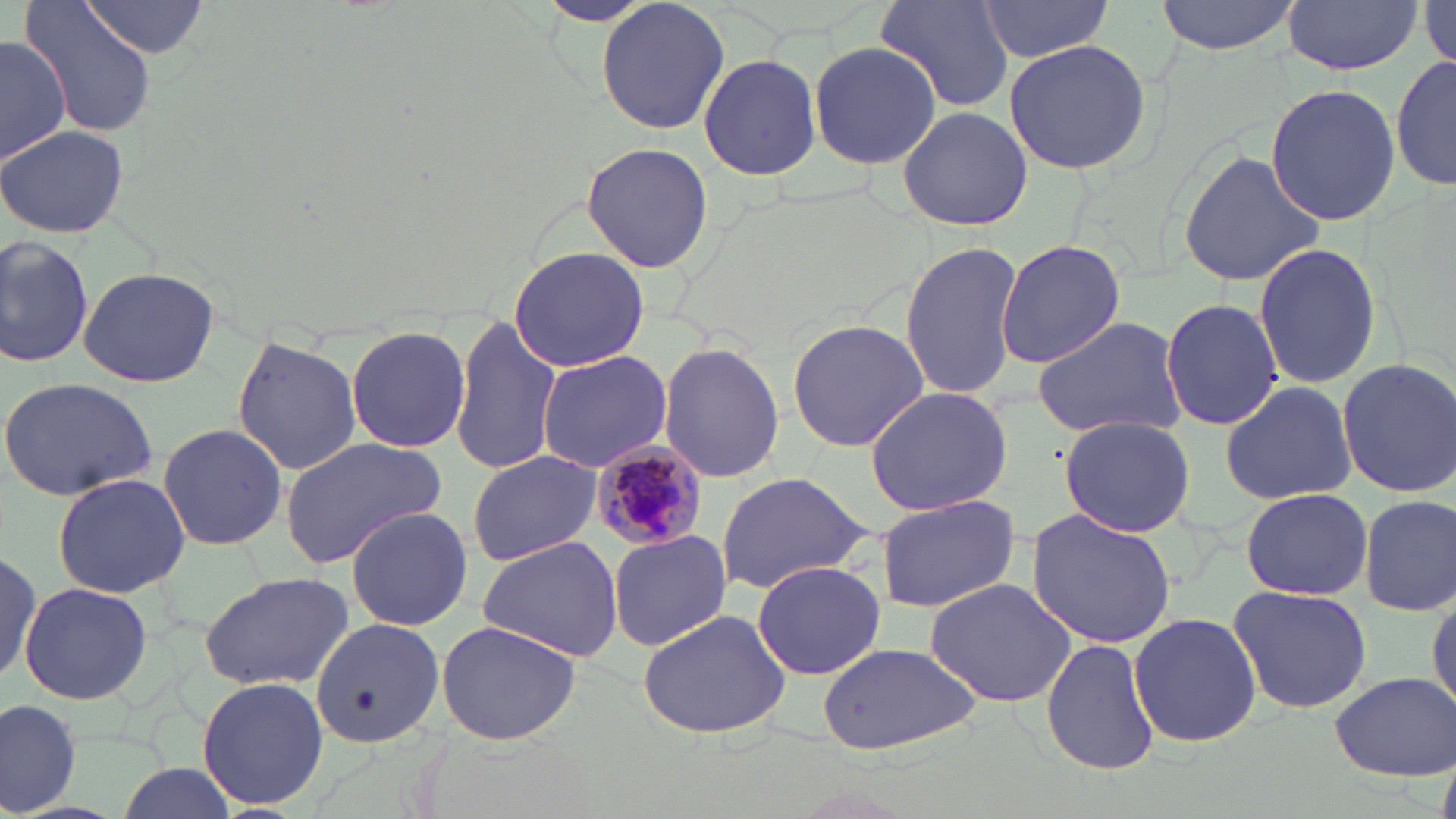
slide-level diagnosis = Plasmodium malariae
preparation = thin blood film
modality = light microscopy
field of view = single
uninfected red blood cell locations = approximate bounding boxes as named x1/y1/x2/y2 corners in pixels: (x1=19, y1=0, x2=157, y2=138), (x1=446, y1=0, x2=583, y2=49), (x1=530, y1=0, x2=663, y2=29), (x1=875, y1=0, x2=1016, y2=113), (x1=1154, y1=0, x2=1301, y2=55), (x1=975, y1=1, x2=1114, y2=60), (x1=1281, y1=1, x2=1424, y2=74), (x1=81, y1=2, x2=211, y2=59), (x1=1419, y1=4, x2=1455, y2=68), (x1=2, y1=31, x2=70, y2=168), (x1=1002, y1=38, x2=1153, y2=177), (x1=808, y1=41, x2=941, y2=170), (x1=1393, y1=53, x2=1455, y2=196), (x1=699, y1=54, x2=821, y2=182), (x1=1265, y1=82, x2=1398, y2=226), (x1=898, y1=104, x2=1032, y2=232), (x1=2, y1=125, x2=128, y2=238), (x1=581, y1=140, x2=712, y2=274), (x1=1178, y1=147, x2=1323, y2=289), (x1=0, y1=233, x2=93, y2=368), (x1=994, y1=239, x2=1128, y2=368), (x1=899, y1=241, x2=1023, y2=401), (x1=1255, y1=242, x2=1385, y2=387), (x1=506, y1=246, x2=651, y2=372), (x1=78, y1=267, x2=221, y2=388), (x1=1160, y1=297, x2=1284, y2=431), (x1=450, y1=316, x2=561, y2=476), (x1=1030, y1=316, x2=1186, y2=440), (x1=787, y1=317, x2=930, y2=453), (x1=345, y1=325, x2=472, y2=453), (x1=231, y1=336, x2=363, y2=473), (x1=658, y1=342, x2=785, y2=484), (x1=537, y1=350, x2=671, y2=471), (x1=1336, y1=357, x2=1456, y2=500), (x1=1, y1=375, x2=159, y2=503), (x1=1218, y1=380, x2=1357, y2=504), (x1=863, y1=385, x2=1014, y2=517), (x1=1057, y1=416, x2=1197, y2=536), (x1=156, y1=422, x2=289, y2=549), (x1=277, y1=435, x2=448, y2=569), (x1=466, y1=449, x2=601, y2=565), (x1=50, y1=471, x2=190, y2=598), (x1=713, y1=472, x2=876, y2=595), (x1=1240, y1=486, x2=1372, y2=601), (x1=876, y1=494, x2=1021, y2=613), (x1=1360, y1=494, x2=1456, y2=617), (x1=345, y1=505, x2=473, y2=631), (x1=1026, y1=508, x2=1176, y2=649), (x1=606, y1=530, x2=732, y2=651), (x1=476, y1=534, x2=625, y2=663), (x1=0, y1=548, x2=40, y2=692), (x1=751, y1=560, x2=885, y2=680), (x1=199, y1=569, x2=353, y2=689), (x1=923, y1=577, x2=1076, y2=708), (x1=19, y1=581, x2=152, y2=703), (x1=1226, y1=583, x2=1373, y2=717), (x1=1428, y1=589, x2=1455, y2=719), (x1=636, y1=607, x2=794, y2=740), (x1=1130, y1=609, x2=1261, y2=748), (x1=311, y1=617, x2=445, y2=752), (x1=437, y1=620, x2=582, y2=747), (x1=1041, y1=637, x2=1161, y2=775), (x1=816, y1=642, x2=987, y2=756), (x1=1329, y1=672, x2=1453, y2=780), (x1=196, y1=676, x2=329, y2=810), (x1=1, y1=696, x2=81, y2=816)
Plasmodium malariae-infected red blood cell locations = approximate bounding boxes as named x1/y1/x2/y2 corners in pixels: (x1=586, y1=439, x2=707, y2=554)
stain = May-Grünwald-Giemsa
magnification = 1000x
image size = 1456×819 pixels